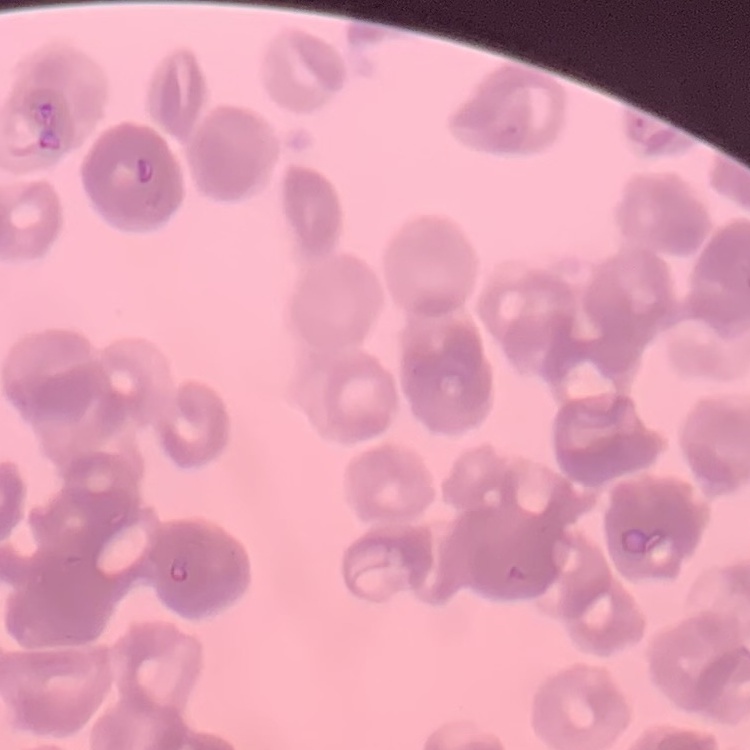

Summary:
  - Red blood cell morphology: rouleaux formation
  - Preparation: thin blood smear
  - Stain: Field's or Giemsa
  - Image type: square crop of a larger photomicrograph